Outline each blood parasite and name the species.
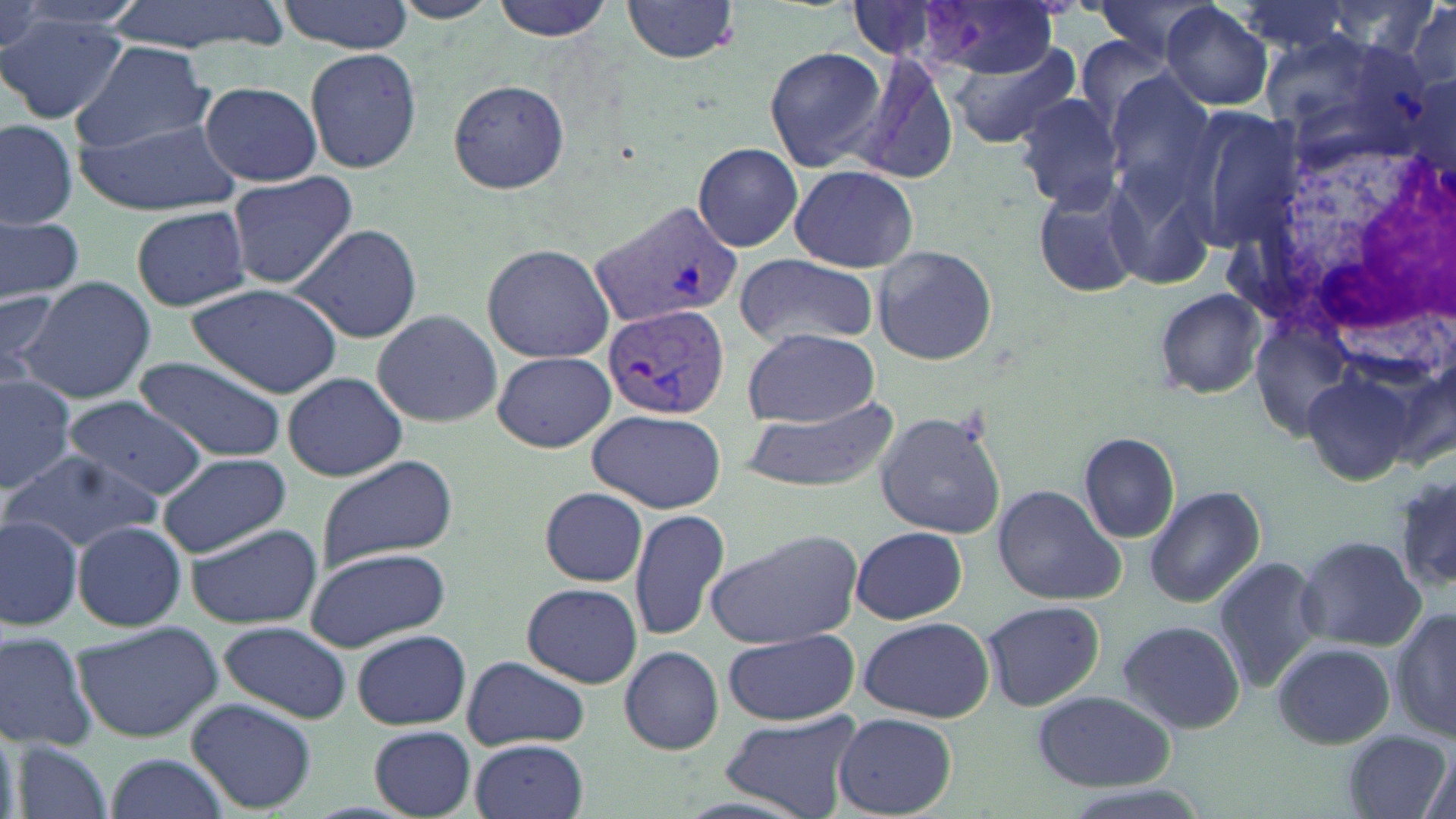
Approximate bounding boxes as [x1, y1, x2, y2] in pixels.
Plasmodium vivax-infected red blood cells: [592, 203, 744, 330], [600, 302, 732, 423].
No Plasmodium falciparum, Plasmodium ovale, Plasmodium malariae, Babesia divergens, or Trypanosoma brucei observed.

slide-level diagnosis = Plasmodium vivax
uninfected red blood cell locations = approximate bounding boxes as [x1, y1, x2, y2] in pixels: [106, 0, 290, 55], [392, 0, 497, 24], [489, 0, 620, 42], [621, 0, 743, 64], [1088, 0, 1221, 64], [277, 1, 414, 52], [1403, 1, 1456, 93], [920, 2, 1062, 76], [1160, 3, 1273, 110], [0, 12, 128, 125], [1260, 30, 1425, 159], [71, 41, 217, 154], [946, 41, 1078, 149], [763, 45, 886, 172], [303, 47, 424, 174], [853, 55, 960, 186], [1101, 73, 1217, 209], [446, 77, 569, 196], [198, 80, 323, 187], [1013, 92, 1127, 210], [1180, 106, 1306, 252], [0, 118, 79, 229], [77, 118, 241, 213], [693, 142, 804, 253], [1100, 160, 1218, 294], [790, 165, 918, 271], [223, 169, 360, 290], [1030, 175, 1146, 300], [131, 204, 252, 311], [0, 216, 83, 300], [288, 223, 421, 345], [482, 242, 616, 363], [872, 245, 997, 366], [733, 255, 879, 348], [12, 277, 157, 403], [184, 283, 343, 397], [1152, 287, 1267, 400], [0, 290, 61, 370], [371, 310, 504, 427], [740, 328, 881, 426], [492, 350, 615, 453], [135, 356, 286, 463], [0, 371, 81, 494], [283, 371, 407, 481], [1307, 375, 1411, 486], [65, 396, 207, 500], [740, 397, 901, 494], [588, 407, 729, 513], [875, 409, 1007, 539], [1078, 432, 1181, 543], [4, 449, 164, 551], [156, 452, 290, 557], [315, 457, 460, 573], [1394, 470, 1456, 591], [992, 485, 1125, 606], [1145, 485, 1265, 609], [538, 486, 648, 587], [628, 506, 730, 642], [0, 513, 85, 632], [72, 521, 186, 632], [184, 523, 322, 630], [851, 526, 968, 625], [706, 530, 862, 649], [1295, 536, 1425, 649], [303, 546, 452, 652], [1210, 555, 1324, 692], [521, 582, 643, 689], [980, 600, 1105, 712], [1392, 605, 1454, 747], [859, 616, 993, 722], [70, 620, 225, 743], [218, 621, 351, 721], [1116, 621, 1246, 732], [350, 628, 471, 730], [1, 629, 96, 751], [720, 629, 859, 723], [1270, 642, 1394, 750], [620, 647, 723, 754], [460, 657, 589, 750], [1032, 690, 1175, 789], [186, 698, 317, 813], [721, 710, 861, 818], [834, 712, 957, 816], [0, 717, 21, 819], [369, 727, 476, 817], [1340, 727, 1451, 819], [471, 739, 589, 819], [16, 741, 117, 819], [1417, 750, 1455, 819], [103, 753, 229, 818]
stain = May-Grünwald-Giemsa
field of view = single
magnification = 1000x
modality = optical microscopy
white blood cell locations = approximate bounding boxes as [x1, y1, x2, y2] in pixels: [1289, 145, 1454, 349]
image size = 1456×819 pixels
preparation = thin blood film